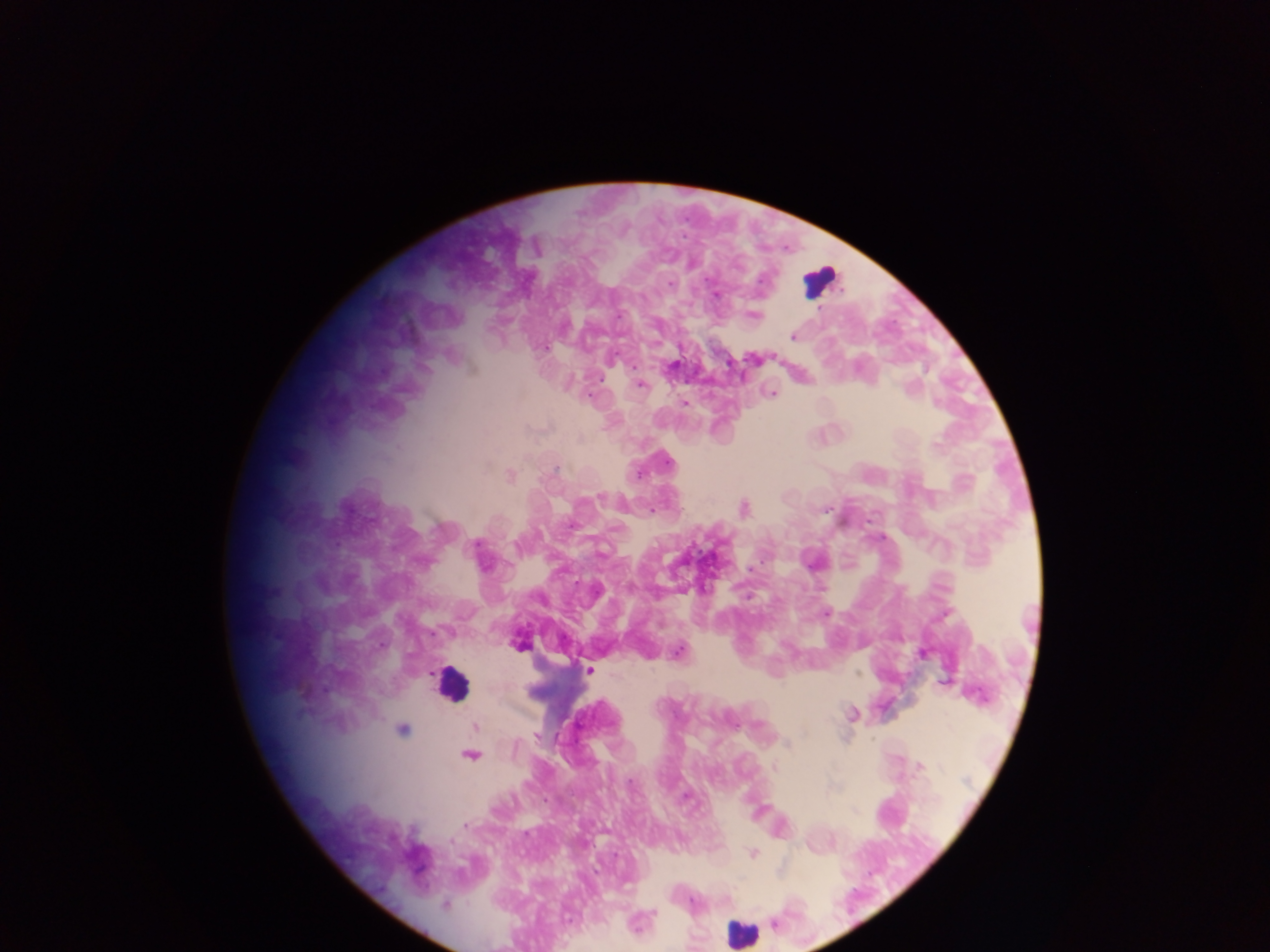

preparation = thick blood film
country = Ghana
leukocyte locations = approximate centers as [x, y] in pixels: [820, 281], [455, 682], [736, 924]
capture = mobile-phone photograph through a microscope
field of view = single
image size = 1270×952 pixels
Plasmodium parasite locations = approximate centers as [x, y] in pixels: [626, 230], [671, 254], [694, 264], [669, 282], [842, 290], [717, 294], [753, 315], [792, 336], [545, 349], [753, 359], [729, 368], [923, 370], [857, 371], [571, 380], [640, 384], [911, 389], [771, 391], [685, 402], [937, 404], [936, 443], [552, 470], [510, 476], [598, 500], [743, 509], [871, 519], [880, 536], [480, 541], [518, 541], [751, 567], [750, 597], [827, 612], [247, 635], [519, 645], [676, 651], [924, 654], [590, 670], [859, 673], [431, 674], [944, 681], [851, 712], [727, 720], [754, 726], [475, 727], [403, 729], [805, 730], [538, 737], [784, 743], [515, 747], [469, 755], [920, 767], [685, 799], [464, 825], [831, 841], [752, 853], [655, 912], [773, 923]